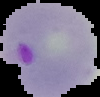 Image is 100×97 pixels. Result: malaria parasites identified. From a thin blood film. Segmented cell region on a black background.